Name the blood parasite species.
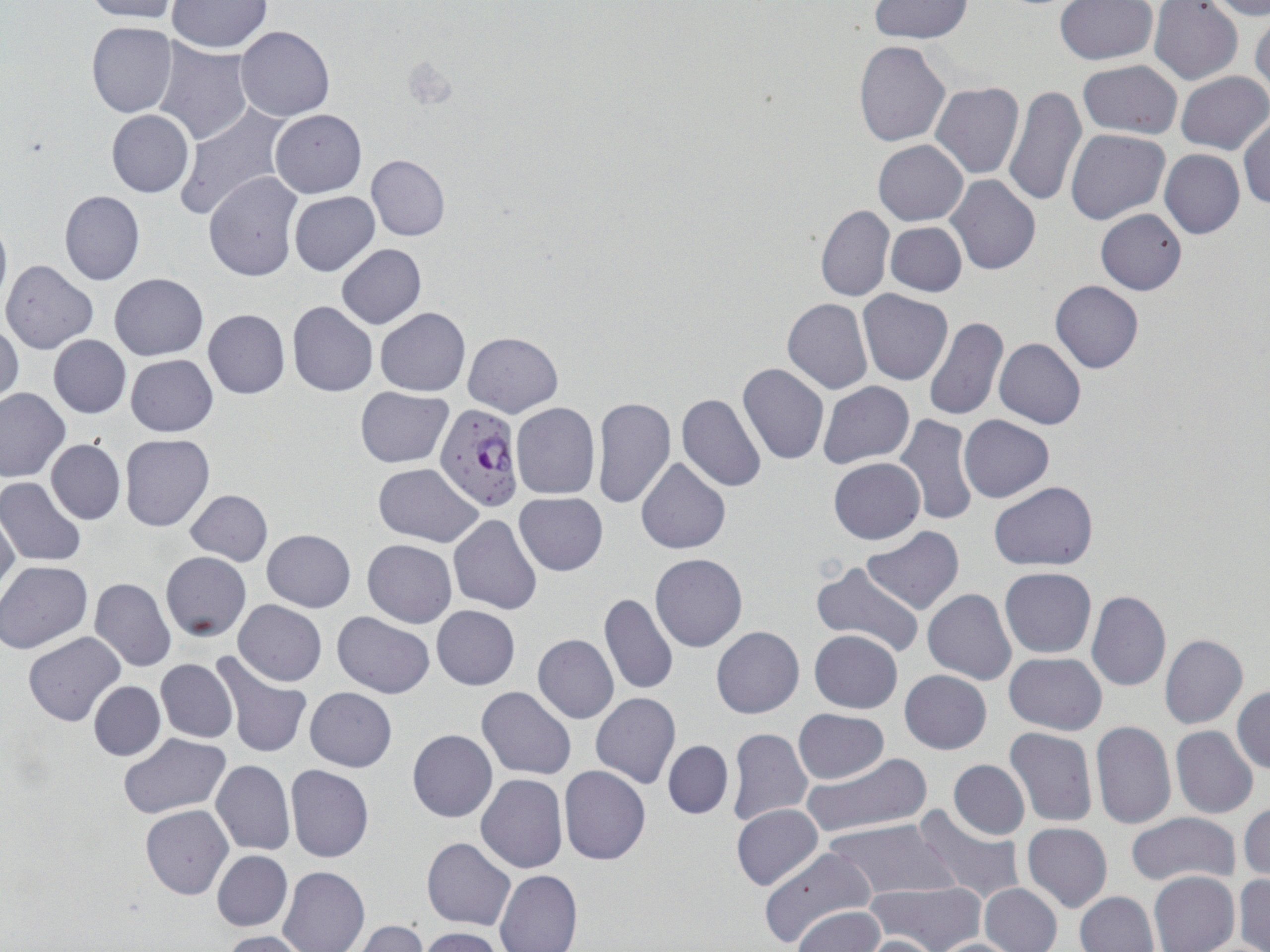
Plasmodium falciparum.

{
  "modality": "optical microscopy",
  "preparation": "thin blood smear",
  "field_of_view": "one of a larger specimen",
  "stain": "May-Grünwald-Giemsa",
  "image_size": "1270×952 pixels",
  "plasmodium_falciparum_infected_red_blood_cell_locations": "approximate bounding boxes as [x1, y1, x2, y2] in pixels: [435, 403, 524, 511]",
  "uninfected_red_blood_cell_locations": "approximate bounding boxes as [x1, y1, x2, y2] in pixels: [82, 0, 181, 23], [168, 1, 271, 53], [868, 1, 972, 43], [1054, 1, 1157, 66], [1149, 1, 1243, 85], [1202, 1, 1270, 20], [1250, 12, 1270, 104], [86, 21, 177, 118], [236, 26, 333, 121], [152, 40, 254, 146], [853, 41, 950, 146], [1078, 60, 1183, 138], [1177, 71, 1269, 153], [931, 83, 1024, 179], [1004, 84, 1087, 208], [174, 105, 291, 220], [106, 110, 194, 197], [271, 110, 365, 197], [1239, 112, 1269, 212], [1067, 130, 1169, 225], [873, 140, 968, 225], [1160, 149, 1245, 239], [366, 154, 450, 241], [202, 171, 302, 282], [945, 176, 1041, 277], [59, 190, 144, 285], [288, 191, 380, 276], [816, 205, 894, 302], [1096, 208, 1187, 294], [0, 215, 11, 315], [885, 222, 966, 296], [336, 243, 426, 329], [1, 260, 99, 354], [109, 274, 207, 359], [1050, 280, 1144, 373], [857, 290, 954, 385], [782, 298, 872, 394], [287, 301, 377, 396], [203, 308, 290, 398], [375, 308, 470, 396], [922, 317, 1007, 421], [0, 322, 22, 406], [464, 331, 563, 417], [48, 336, 131, 417], [995, 338, 1086, 430], [126, 354, 218, 437], [737, 364, 829, 466], [818, 381, 915, 468], [0, 386, 69, 482], [355, 387, 452, 468], [677, 394, 767, 493], [592, 396, 676, 510], [511, 403, 602, 499], [894, 414, 978, 528], [959, 415, 1053, 502], [120, 433, 214, 531], [45, 439, 124, 524], [636, 458, 731, 554], [829, 458, 925, 544], [374, 463, 484, 547], [0, 478, 86, 566], [989, 482, 1098, 572], [185, 489, 273, 566], [515, 491, 607, 576], [0, 508, 20, 603], [448, 514, 543, 614], [863, 527, 964, 614], [261, 529, 354, 612], [362, 539, 457, 627], [161, 552, 251, 640], [650, 554, 748, 651], [1, 561, 93, 653], [809, 561, 923, 662], [93, 562, 247, 653], [999, 567, 1097, 658], [90, 577, 177, 672], [923, 589, 1016, 685], [1087, 589, 1171, 691], [600, 592, 677, 696], [234, 599, 327, 685], [432, 605, 520, 690], [332, 613, 434, 699], [711, 626, 804, 717], [809, 630, 902, 713], [24, 632, 125, 726], [533, 634, 618, 723], [1160, 634, 1248, 730], [216, 651, 313, 757], [1004, 652, 1107, 734], [156, 659, 237, 743], [899, 670, 993, 754], [89, 681, 165, 760], [1232, 685, 1270, 775], [306, 686, 397, 770], [476, 686, 576, 779], [591, 693, 680, 789], [793, 708, 889, 784], [1090, 721, 1175, 829], [1171, 726, 1257, 818], [1005, 727, 1097, 827], [727, 728, 812, 828], [407, 729, 496, 823], [120, 733, 231, 819], [663, 741, 733, 818], [801, 753, 931, 838], [948, 759, 1029, 839], [211, 760, 295, 855], [286, 765, 373, 862], [560, 766, 651, 864], [475, 774, 567, 873], [1239, 801, 1270, 883], [731, 804, 823, 891], [140, 805, 233, 900], [912, 805, 1024, 905], [1125, 811, 1241, 888], [825, 817, 956, 902], [1021, 822, 1112, 912], [422, 838, 516, 931], [758, 846, 879, 948], [211, 850, 291, 932], [279, 866, 369, 952], [494, 869, 582, 952], [1148, 871, 1239, 952], [1233, 875, 1270, 952], [868, 879, 987, 952], [980, 883, 1061, 952], [1074, 891, 1159, 952], [793, 906, 884, 952], [349, 921, 428, 952], [419, 927, 508, 952], [218, 930, 312, 952], [859, 934, 942, 952], [928, 938, 1027, 951]",
  "magnification": "1000x"
}